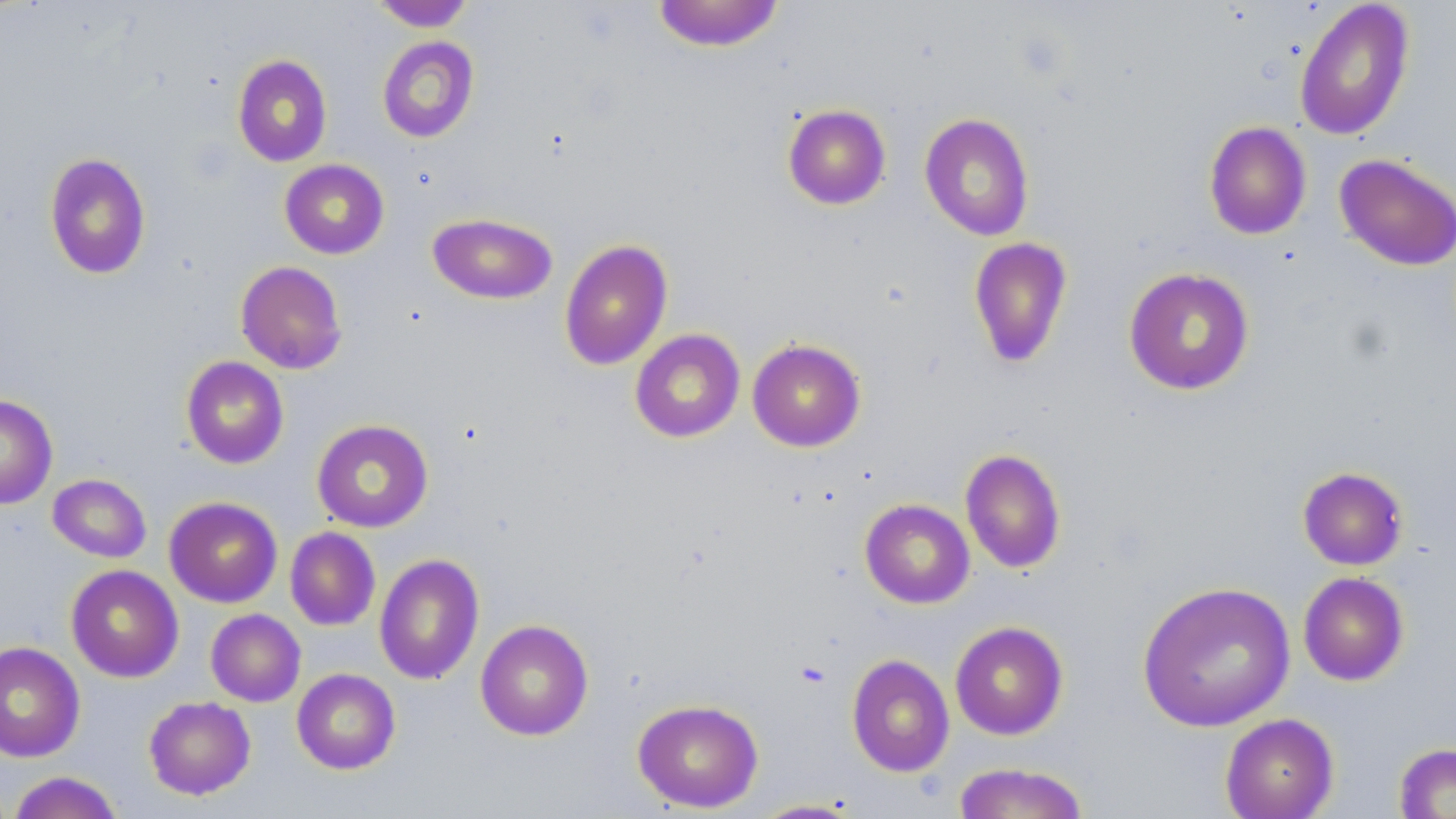
{
  "slide_level_diagnosis": "negative for blood parasites",
  "image_size": "1456×819 pixels",
  "field_of_view": "single",
  "preparation": "thin blood smear",
  "stain": "May-Grünwald-Giemsa",
  "modality": "light microscopy",
  "magnification": "1000x",
  "uninfected_red_blood_cell_locations": "approximate bounding boxes as (x1, y1, x2, y2) in pixels: (653, 0, 784, 52), (370, 1, 475, 32), (1294, 1, 1416, 141), (376, 36, 480, 143), (232, 54, 332, 167), (782, 104, 891, 210), (919, 112, 1034, 241), (1204, 121, 1312, 240), (44, 152, 151, 280), (1334, 153, 1456, 272), (279, 159, 389, 259), (427, 212, 557, 305), (968, 237, 1073, 368), (559, 239, 673, 371), (235, 261, 347, 374), (1123, 267, 1255, 395), (629, 329, 745, 443), (747, 338, 866, 452), (181, 356, 289, 469), (0, 394, 58, 509), (311, 419, 434, 532), (960, 448, 1066, 573), (1297, 466, 1409, 570), (47, 474, 151, 563), (164, 496, 283, 608), (859, 499, 975, 609), (285, 527, 380, 631), (374, 553, 485, 685), (65, 564, 184, 682), (1297, 571, 1410, 686), (1137, 581, 1296, 732), (206, 609, 305, 707), (475, 619, 594, 741), (949, 620, 1069, 740), (0, 641, 85, 763), (846, 653, 955, 777), (292, 668, 400, 774), (143, 696, 256, 800), (632, 698, 764, 813), (1219, 713, 1339, 819), (1393, 742, 1456, 818), (952, 762, 1089, 818), (6, 771, 124, 819), (749, 799, 865, 818)"
}